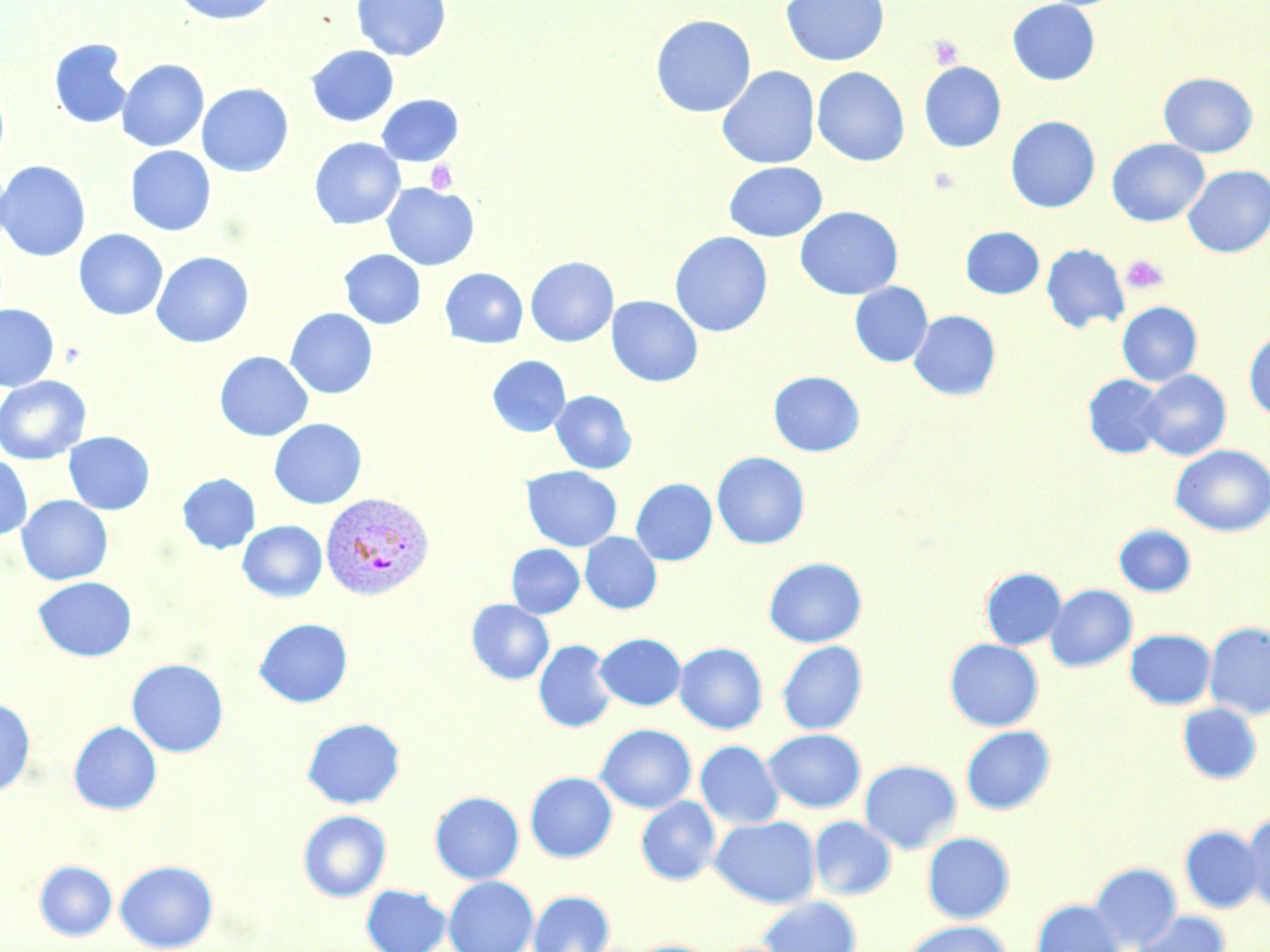 Approximate bounding boxes as (x1,y1)-(x2,y2) corner pairs in pixels. Plasmodium vivax-infected red blood cell locations: (320,491)-(434,601). Platelet locations: (928,35)-(964,69), (425,161)-(459,194), (1120,254)-(1169,295). Uninfected red blood cell locations: (170,0)-(280,26), (351,0)-(451,61), (780,0)-(889,67), (1007,0)-(1100,86), (650,14)-(756,118), (49,38)-(133,130), (306,45)-(399,127), (116,59)-(209,152), (918,61)-(1006,152), (716,66)-(820,169), (812,66)-(910,167), (1158,72)-(1258,157), (0,79)-(10,176), (196,83)-(294,177), (376,94)-(464,167), (1005,116)-(1100,212), (309,137)-(405,230), (1106,138)-(1209,226), (125,146)-(217,236), (0,160)-(91,262), (723,161)-(827,242), (1183,165)-(1270,257), (382,182)-(480,271), (795,206)-(902,300), (961,226)-(1044,299), (74,229)-(168,320), (670,231)-(773,337), (1041,243)-(1129,332), (339,249)-(425,329), (151,251)-(254,348), (525,256)-(619,346), (440,268)-(528,348), (849,282)-(932,367), (606,295)-(703,387), (1117,302)-(1202,386), (0,303)-(59,391), (285,308)-(377,399), (909,310)-(1001,400), (1244,330)-(1270,420), (214,351)-(313,441), (487,355)-(570,437), (1139,369)-(1231,461), (768,370)-(865,457), (1083,374)-(1167,459), (0,375)-(91,464), (551,390)-(637,474), (268,418)-(367,509), (63,431)-(155,515), (1170,445)-(1270,536), (711,451)-(810,549), (0,455)-(32,540), (522,466)-(622,551), (177,473)-(261,553), (631,478)-(717,565), (16,495)-(113,585), (238,520)-(327,602), (1114,524)-(1195,596), (580,532)-(661,614), (506,544)-(585,618), (764,557)-(867,647), (981,567)-(1066,650), (33,576)-(136,661), (1045,584)-(1137,672), (466,599)-(554,684), (253,618)-(353,708), (1204,623)-(1270,720), (1125,629)-(1216,709), (594,632)-(686,710), (945,639)-(1044,731), (533,640)-(617,733), (777,640)-(867,735), (674,642)-(767,734), (127,658)-(229,757), (0,697)-(35,797), (1177,703)-(1262,784), (302,717)-(405,809), (68,721)-(162,814), (595,724)-(696,814), (961,726)-(1056,815), (763,729)-(866,813), (695,740)-(783,829), (859,759)-(962,854), (525,771)-(617,863), (430,791)-(524,884), (636,796)-(720,885), (298,809)-(391,901), (1243,811)-(1270,913), (710,815)-(820,908), (809,815)-(897,900), (1180,826)-(1265,913), (922,832)-(1015,923), (34,860)-(117,941), (115,860)-(219,952), (1088,862)-(1182,951), (443,875)-(538,952), (361,884)-(452,952), (528,890)-(615,952), (758,896)-(862,952), (1032,899)-(1125,952), (1130,911)-(1231,952), (901,920)-(1011,952), (624,939)-(718,952). Slide-level diagnosis: Plasmodium vivax. Thin blood film. Image is 1270×952 pixels. May-Grünwald-Giemsa stain. Optical microscopy. Captured at 1000x magnification. Single field of view.